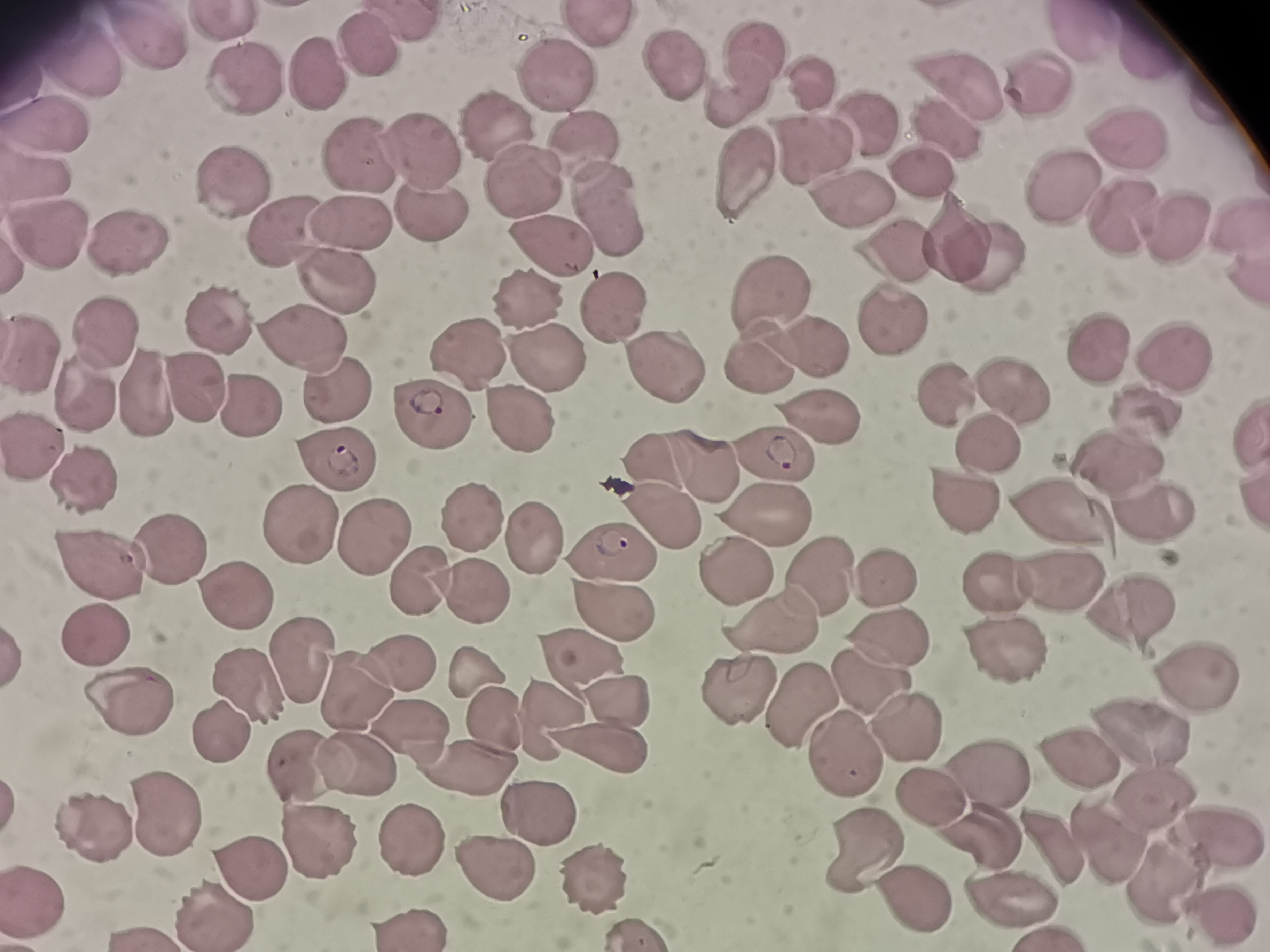

Approximate centers as {x, y} in pixels. Cell locations: {225, 25}, {593, 26}, {1080, 34}, {157, 39}, {365, 47}, {1143, 57}, {759, 62}, {673, 63}, {81, 65}, {551, 73}, {310, 75}, {959, 84}, {248, 87}, {1038, 90}, {812, 92}, {731, 98}, {863, 118}, {500, 127}, {945, 134}, {45, 135}, {583, 142}, {817, 147}, {1133, 147}, {427, 154}, {362, 159}, {917, 175}, {741, 176}, {524, 179}, {227, 180}, {37, 181}, {847, 192}, {1060, 195}, {430, 205}, {609, 208}, {1118, 213}, {1240, 220}, {350, 223}, {279, 230}, {1176, 230}, {55, 235}, {131, 242}, {955, 242}, {550, 246}, {985, 255}, {898, 256}, {1245, 278}, {338, 284}, {775, 291}, {526, 305}, {615, 305}, {221, 322}, {894, 324}, {103, 332}, {306, 341}, {812, 341}, {1096, 349}, {472, 358}, {1177, 359}, {754, 360}, {654, 361}, {542, 367}, {335, 391}, {195, 393}, {948, 396}, {1016, 396}, {151, 397}, {84, 399}, {250, 403}, {424, 408}, {818, 412}, {1142, 421}, {519, 426}, {1253, 429}, {990, 448}, {39, 449}, {771, 456}, {335, 460}, {651, 462}, {1116, 464}, {698, 467}, {88, 482}, {963, 502}, {1251, 502}, {1148, 503}, {761, 515}, {474, 516}, {655, 519}, {299, 522}, {1061, 526}, {368, 536}, {531, 538}, {612, 551}, {169, 552}, {106, 565}, {731, 567}, {822, 572}, {414, 577}, {997, 580}, {886, 583}, {1061, 583}, {465, 591}, {238, 595}, {612, 608}, {781, 617}, {1142, 619}, {88, 632}, {890, 638}, {1009, 647}, {577, 651}, {298, 662}, {398, 663}, {1191, 672}, {475, 674}, {871, 684}, {735, 685}, {247, 687}, {353, 690}, {610, 699}, {794, 699}, {126, 703}, {554, 715}, {493, 723}, {1134, 726}, {906, 727}, {221, 732}, {404, 732}, {606, 750}, {838, 756}, {1072, 760}, {310, 763}, {357, 765}, {472, 765}, {983, 775}, {929, 792}, {1159, 799}, {535, 808}, {162, 815}, {1214, 825}, {100, 832}, {986, 833}, {1103, 833}, {316, 834}, {866, 840}, {407, 842}, {1053, 851}, {492, 863}, {594, 871}, {256, 873}, {1166, 876}, {1013, 891}, {905, 893}, {35, 895}, {208, 910}, {410, 923}, {137, 931}. Giemsa stain. Thin blood smear. Photographed with a smartphone camera at the microscope eyepiece. One field from this slide. Image is 1270×952 pixels.